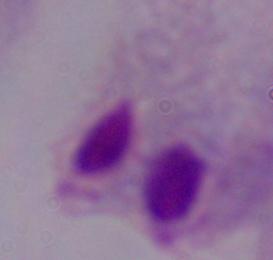
Summary:
  - Identification: trichomonad
  - Magnification: 1000x
  - Modality: photomicrograph